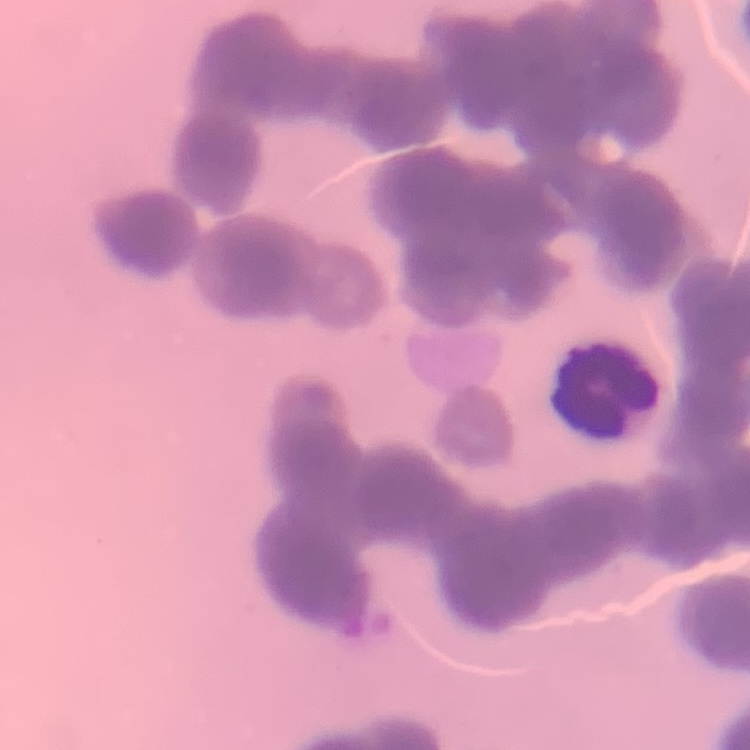
erythrocyte morphology = rouleaux formation
preparation = thin blood smear
stain = Field's or Giemsa
image type = square crop of a larger photomicrograph